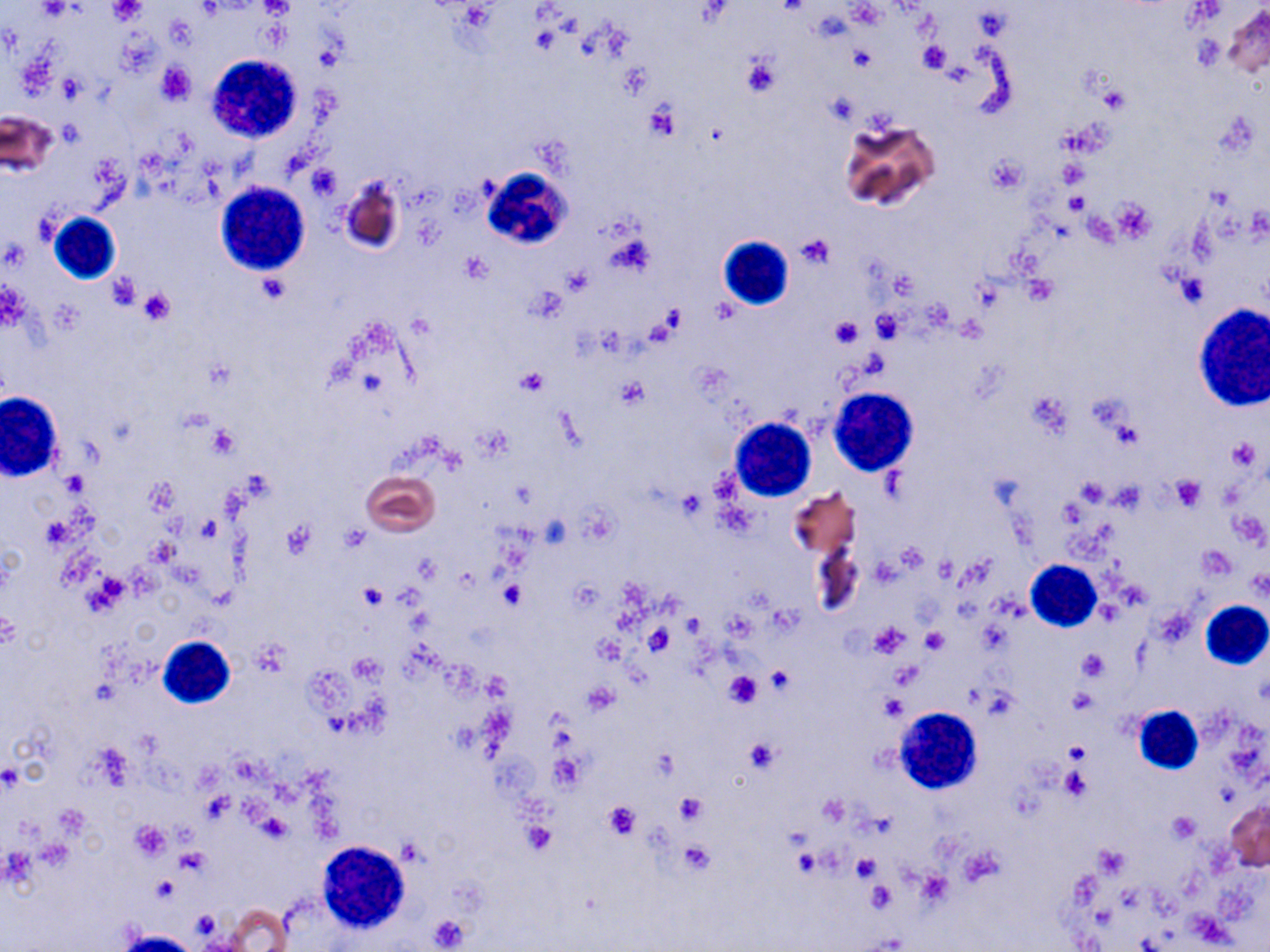
Summary:
  - Coordinate format: approximate bounding boxes as (x1,y1)-(x2,y2) corner pairs in pixels
  - Uninfected red blood cell locations: (1217,5)-(1270,80), (0,109)-(58,178), (839,117)-(940,211), (339,174)-(405,255), (361,471)-(439,535), (789,487)-(859,561), (809,536)-(865,621), (1227,800)-(1270,870), (222,903)-(293,951)
  - Platelet locations: (260,0)-(293,19), (38,1)-(73,21), (109,1)-(145,25), (846,3)-(883,27), (917,42)-(950,73), (848,47)-(875,73), (740,52)-(782,97), (157,62)-(194,105), (621,63)-(653,95), (56,75)-(85,102), (1098,83)-(1131,114), (645,101)-(679,139), (56,120)-(85,146), (985,157)-(1025,194), (1059,160)-(1087,188), (306,164)-(341,200), (1066,191)-(1086,217), (1112,199)-(1154,242), (797,234)-(834,268), (462,255)-(491,282), (1176,270)-(1209,308), (107,273)-(143,311), (138,287)-(176,324), (528,288)-(566,323), (872,311)-(906,341), (830,316)-(861,350), (518,368)-(549,396), (613,378)-(650,410), (207,426)-(239,459), (1227,438)-(1261,471), (61,471)-(88,497), (1170,474)-(1206,511), (1075,479)-(1109,509), (1111,482)-(1145,510), (41,516)-(78,547), (197,516)-(222,539), (282,520)-(316,559), (341,526)-(369,552), (894,544)-(928,575), (1200,546)-(1235,578), (87,571)-(131,611), (499,581)-(525,610), (359,585)-(388,610), (0,611)-(21,649), (870,623)-(910,657), (644,626)-(675,655), (920,628)-(948,653), (253,638)-(292,676), (1079,650)-(1107,679), (765,666)-(792,695), (722,671)-(763,708), (878,695)-(906,721), (744,739)-(781,772), (1063,740)-(1089,763), (550,755)-(584,791), (1060,768)-(1091,802), (676,794)-(704,823), (603,801)-(642,841), (1168,812)-(1200,844), (129,821)-(170,860), (521,821)-(555,855), (678,840)-(714,875), (1094,844)-(1130,878), (177,849)-(210,874), (852,854)-(880,882), (865,881)-(897,913), (428,915)-(470,950)
  - White blood cell locations: (207,52)-(304,142), (479,169)-(578,251), (212,181)-(310,273), (48,213)-(120,285), (717,236)-(795,310), (1192,302)-(1270,414), (829,389)-(917,476), (0,390)-(64,482), (729,417)-(816,501), (1027,559)-(1102,631), (1200,600)-(1270,669), (158,636)-(236,708), (1134,706)-(1203,775), (894,707)-(983,791), (316,840)-(411,933)
  - Slide-level diagnosis: negative for blood parasites
  - Image size: 1270×952 pixels
  - Magnification: 1000x
  - Stain: May-Grünwald-Giemsa
  - Modality: optical microscopy
  - Field of view: single
  - Preparation: thin blood smear